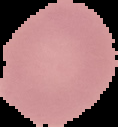
{
  "image_size": "118×127 pixels",
  "image_type": "cell region segmented out of the field of view; surrounding area masked to black",
  "preparation": "thin blood smear",
  "malaria_status": "uninfected"
}